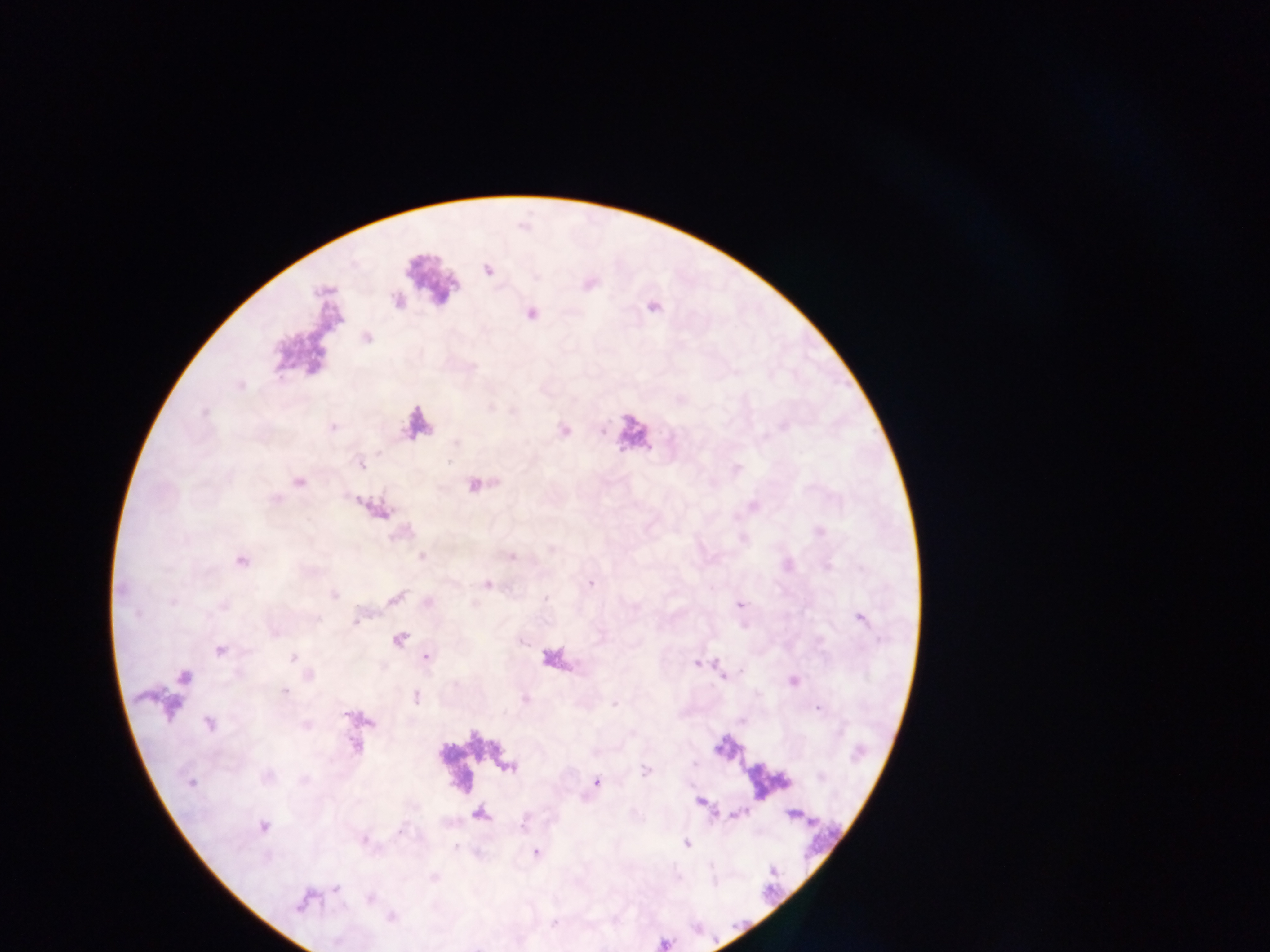

Approximate centers as x y in pixels. Malaria parasite locations: 488 270; 361 465; 299 482; 422 556; 241 561; 591 583; 335 595; 741 604; 861 620; 400 640; 220 650; 427 657; 293 658; 696 664; 183 676; 284 691; 417 697; 615 704; 817 708; 209 723; 353 748; 646 771; 191 783; 597 783; 700 801; 793 815; 263 826; 686 843; 537 853; 336 888; 370 899; 303 901; 392 918. Photographed through a microscope with a mobile-phone camera. Thick blood film. Image is 1270×952 pixels. One field of view. Sample from Ghana.